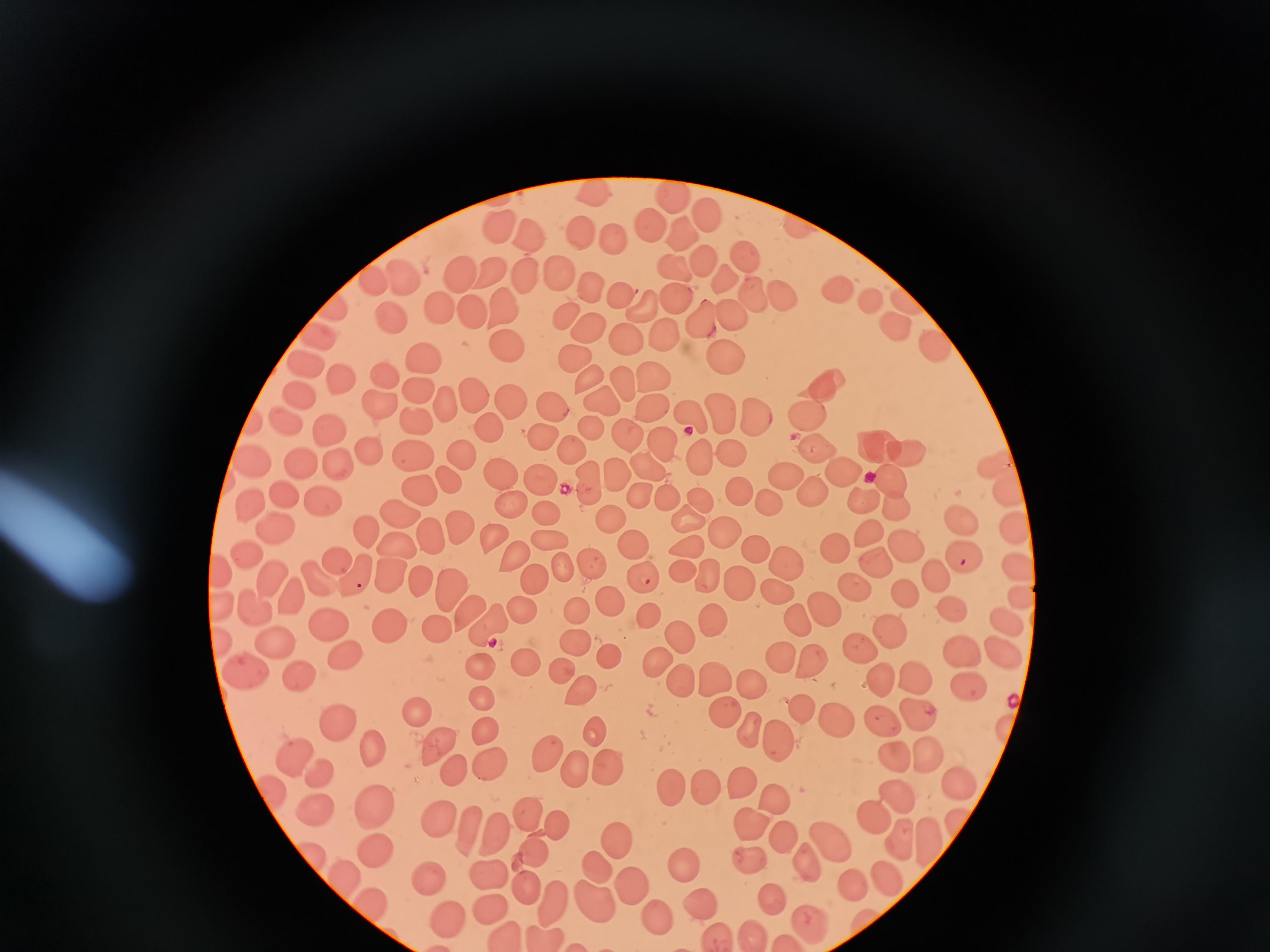
Approximate centers as (x, y) in pixels.
Summary:
  - Cell locations: (597, 190), (675, 197), (713, 218), (650, 222), (502, 224), (803, 229), (530, 233), (586, 234), (684, 235), (613, 240), (747, 257), (704, 263), (675, 269), (462, 271), (494, 272), (405, 274), (556, 275), (525, 277), (373, 278), (725, 279), (589, 287), (621, 292), (836, 292), (779, 294), (754, 296), (678, 299), (871, 301), (648, 302), (910, 302), (503, 305), (439, 306), (472, 307), (331, 308), (731, 311), (568, 312), (392, 318), (704, 321), (896, 324), (597, 331), (663, 333), (317, 336), (630, 339), (934, 344), (506, 347), (571, 353), (423, 356), (723, 359), (307, 364), (384, 372), (648, 373), (585, 374), (340, 380), (619, 381), (823, 387), (417, 390), (469, 393), (301, 395), (506, 398), (378, 403), (602, 403), (447, 404), (549, 407), (650, 407), (720, 410), (802, 412), (693, 415), (746, 416), (255, 421), (287, 421), (415, 421), (485, 425), (588, 426), (327, 429), (624, 430), (541, 435), (661, 440), (866, 442), (814, 443), (568, 448), (900, 449), (413, 452), (370, 453), (463, 455), (729, 455), (337, 460), (997, 460), (251, 461), (304, 464), (697, 464), (649, 467), (613, 468), (843, 469), (499, 473), (782, 477), (445, 478), (541, 478), (587, 479), (890, 479), (1004, 485), (419, 489), (283, 493), (738, 493), (812, 493), (640, 495), (865, 497), (322, 499), (510, 501), (667, 501), (697, 501), (249, 503), (769, 508), (900, 510), (545, 511), (398, 516), (958, 517), (609, 519), (689, 520), (455, 523), (269, 530), (1016, 530), (867, 532), (365, 534), (725, 536), (429, 537), (492, 537), (549, 537), (902, 541), (631, 546), (399, 547), (688, 547), (758, 549), (835, 552), (515, 555), (245, 557), (336, 560), (961, 560), (786, 561), (868, 561), (591, 562), (564, 565), (1018, 567), (219, 568), (681, 570), (268, 577), (356, 577), (643, 577), (391, 578), (714, 578), (933, 578), (314, 579), (537, 579), (420, 581), (737, 584), (448, 587), (852, 589), (905, 592), (773, 593), (289, 594), (1021, 596), (612, 598), (251, 604), (221, 606), (820, 606), (580, 607), (950, 609), (521, 610), (465, 611), (651, 613), (791, 616), (488, 620), (708, 620), (330, 621), (1009, 623), (387, 628), (436, 628), (888, 635), (573, 640), (681, 640), (221, 642), (275, 645), (861, 647), (965, 652), (1003, 652), (344, 653), (610, 657), (785, 657), (522, 660), (655, 660), (812, 665), (480, 666), (558, 671), (245, 673), (911, 675), (296, 676), (716, 678), (747, 680), (877, 681), (684, 684), (971, 686), (581, 692), (478, 698), (914, 708), (802, 709), (415, 711), (721, 712), (841, 720), (885, 721), (335, 723), (591, 727), (1007, 729), (482, 730), (752, 731), (777, 738), (441, 744), (367, 745), (548, 751), (897, 754), (290, 755), (928, 755), (488, 763), (578, 765), (609, 768), (451, 769), (320, 776), (956, 781), (739, 782), (666, 785), (702, 786), (272, 790), (900, 795), (774, 801), (316, 808), (376, 808), (525, 808), (875, 816), (962, 819), (436, 820), (466, 823), (753, 823), (556, 827), (498, 830), (784, 836), (896, 839), (928, 839), (620, 841), (832, 841), (305, 847), (533, 849), (371, 850), (747, 857), (593, 861), (687, 864), (809, 865), (486, 873), (883, 875), (432, 878), (851, 878), (345, 879), (527, 884), (630, 884), (768, 893), (590, 898), (370, 904), (489, 904), (554, 904), (700, 904), (652, 913), (449, 917), (812, 923), (751, 932), (713, 933), (543, 934), (502, 936)
  - Stain: Giemsa
  - Preparation: thin blood smear
  - Field of view: single
  - Image size: 1270×952 pixels
  - Capture: smartphone through the microscope eyepiece